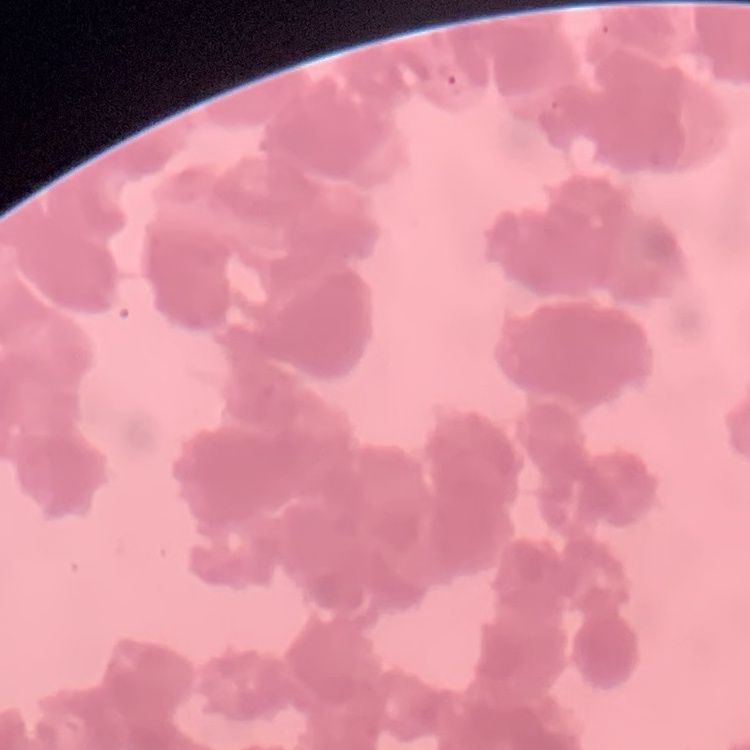 The red blood cells exhibit rouleaux formation. Stained with either Field's or Giemsa. Square crop of a larger photomicrograph. Thin blood smear.